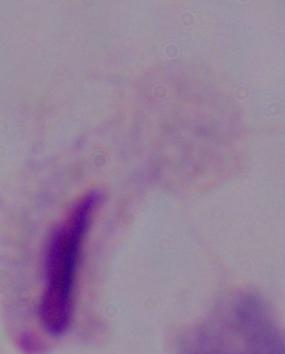

Summary:
  - Modality: photomicrograph
  - Identification: trichomonad
  - Magnification: 1000x